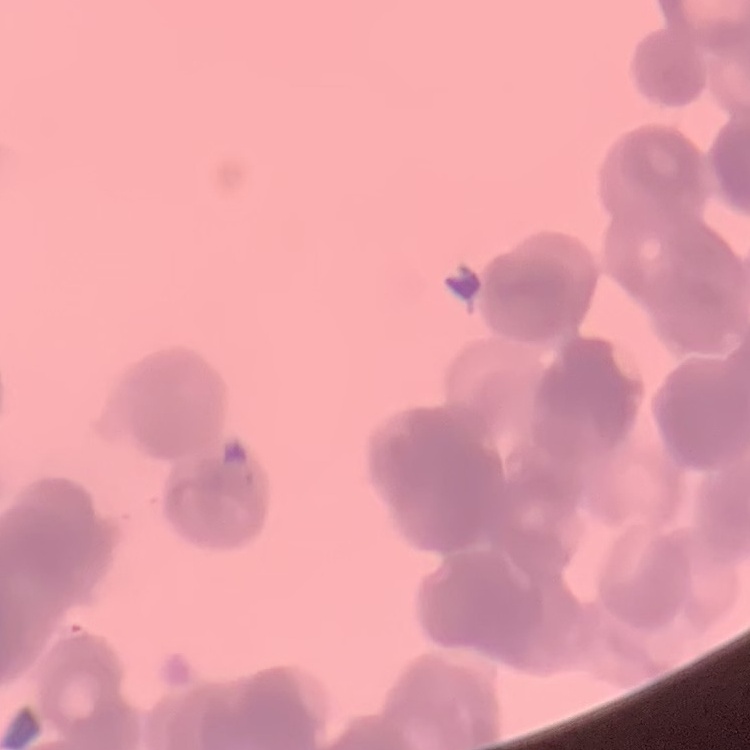
erythrocyte_morphology: rouleaux formation
stain: Field's or Giemsa
image_type: one tile cut from a larger photomicrograph
preparation: thin peripheral smear